Classify this cell by malaria status.
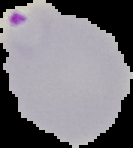

It is parasitized.

Summary:
  - Image type: segmented cell region with the area outside set to black
  - Preparation: thin blood film
  - Image size: 133×148 pixels